Locate every leukocyte (white blood cell).
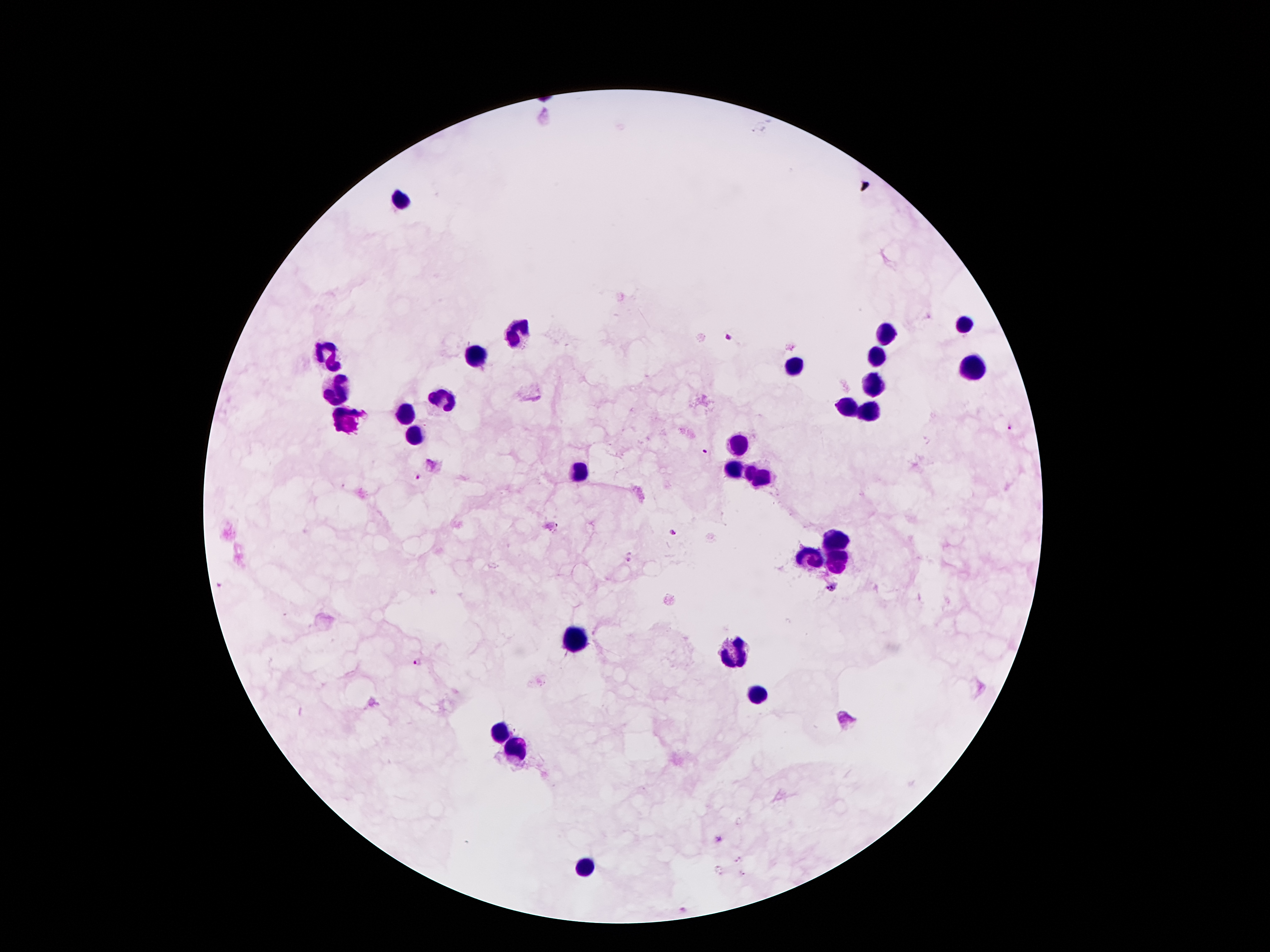
Approximate centers as [x, y] in pixels.
Leukocytes: [404, 198], [962, 326], [518, 331], [884, 331], [328, 354], [476, 356], [876, 356], [792, 366], [972, 366], [871, 383], [337, 391], [439, 398], [849, 406], [868, 408], [407, 415], [345, 420], [416, 438], [737, 442], [733, 470], [579, 474], [758, 477], [836, 541], [809, 558], [834, 561], [575, 642], [737, 653], [757, 695], [501, 731], [515, 752], [584, 867].

Plasmodium parasite locations = [726, 338], [1009, 428], [704, 449], [418, 477], [671, 531], [630, 560], [832, 588], [421, 663], [716, 840], [739, 860], [718, 871], [743, 873]
preparation = thick blood smear
patient malaria status = infected with Plasmodium falciparum
capture = smartphone through the microscope eyepiece
stain = Giemsa
magnification = 100x
field of view = single
image size = 1270×952 pixels